Assess for malaria.
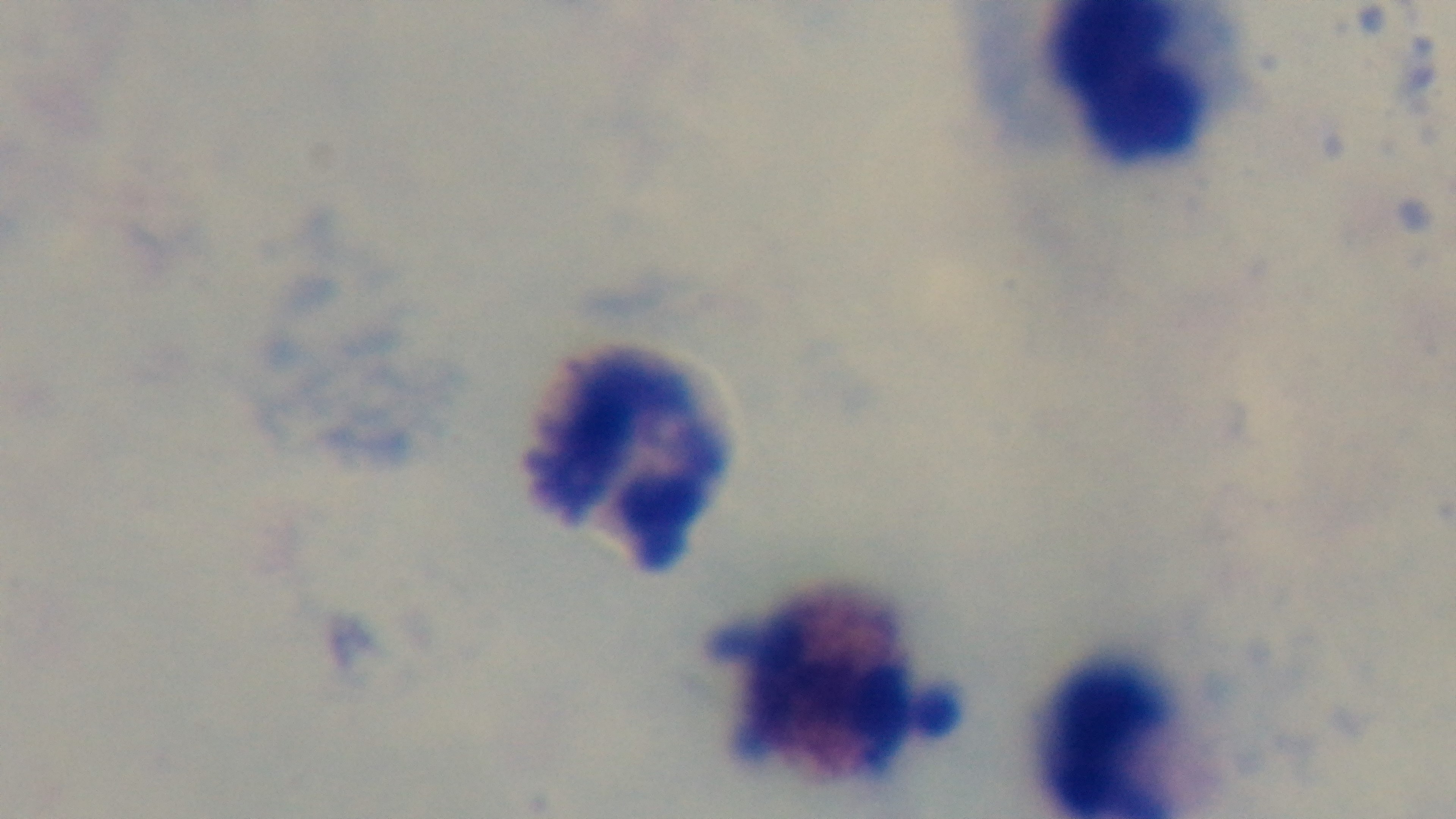

It is uninfected.

{
  "objective": "100x oil immersion",
  "stain": "Giemsa",
  "modality": "light microscopy",
  "field_of_view": "one from the slide",
  "preparation": "thick",
  "capture": "mounted 4K digital camera"
}